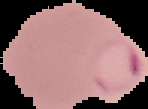
{
  "preparation": "thin blood smear",
  "malaria_status": "parasitized",
  "image_size": "148×109 pixels",
  "image_type": "segmented cell region with the area outside set to black"
}